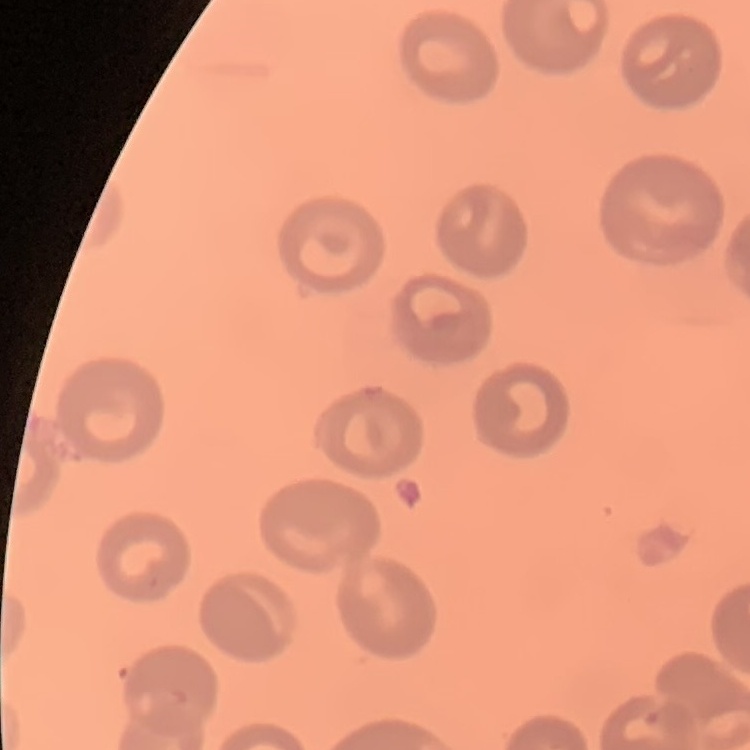

red blood cell morphology = no rouleaux formation
image type = one tile cut from a larger photomicrograph
stain = Field's or Giemsa
preparation = thin peripheral smear